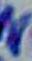

Micrograph. Toxoplasma gondii is shown. Captured at 1000x magnification.